Report the malaria status of this cell.
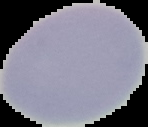
Uninfected.

Image is 148×127 pixels. From a thin blood film. Cell region segmented out of the field of view; the surrounding area is masked to black.